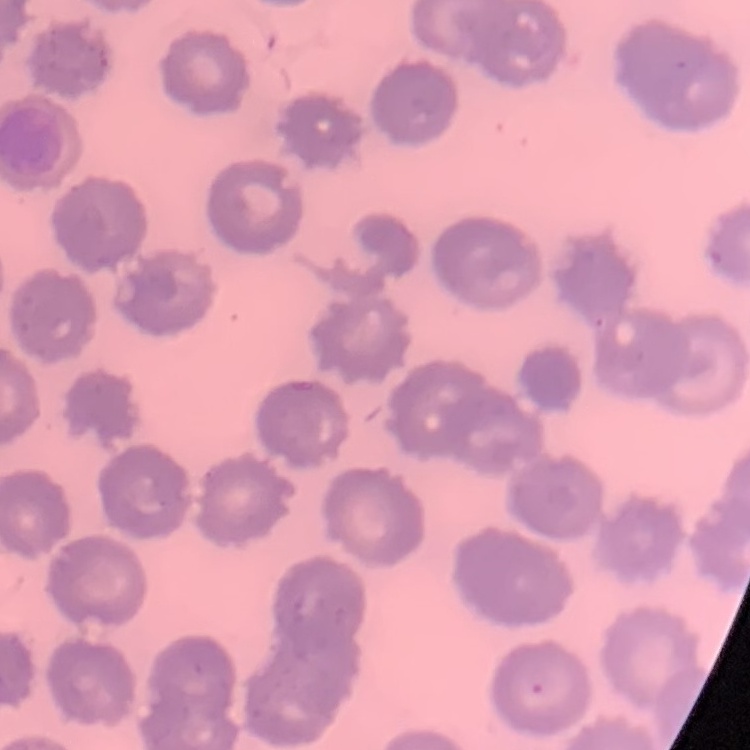

red_blood_cell_morphology: no rouleaux formation
preparation: thin peripheral smear
stain: Field's or Giemsa
image_type: one tile cut from a larger photomicrograph